Point out each leukocyte.
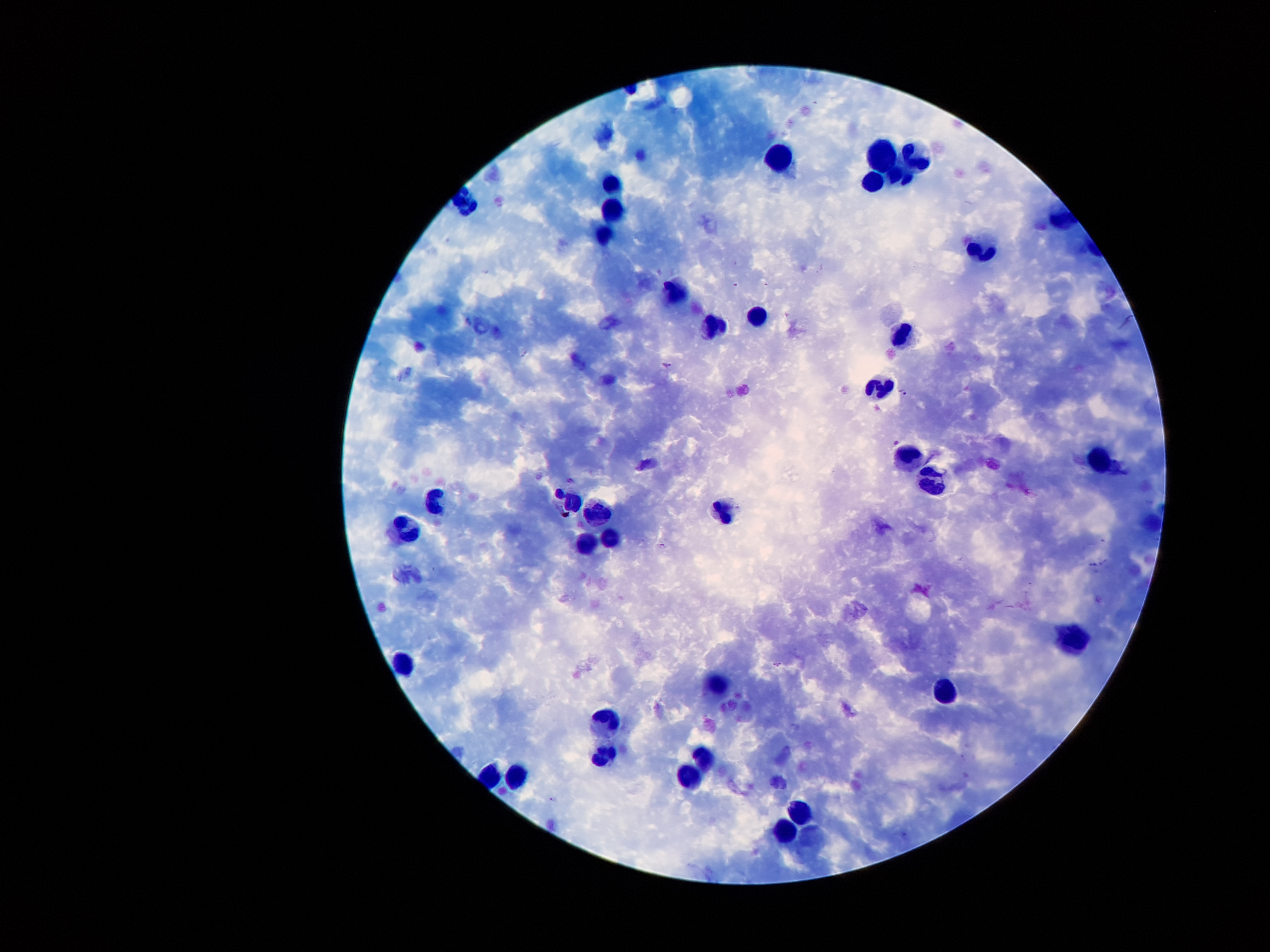

Approximate object centers, in pixels from the top-left corner.
Leukocytes: (x=883, y=155), (x=915, y=156), (x=777, y=163), (x=901, y=175), (x=873, y=180), (x=610, y=182), (x=614, y=212), (x=606, y=235), (x=983, y=251), (x=675, y=295), (x=757, y=318), (x=715, y=323), (x=903, y=337), (x=879, y=388), (x=908, y=455), (x=1094, y=459), (x=931, y=483), (x=435, y=499), (x=571, y=501), (x=723, y=505), (x=595, y=508), (x=408, y=531), (x=611, y=538), (x=587, y=546), (x=1072, y=638), (x=408, y=666), (x=719, y=686), (x=946, y=689), (x=605, y=726), (x=604, y=755), (x=700, y=756), (x=689, y=777), (x=516, y=780), (x=799, y=813), (x=787, y=831).

malaria parasite locations = (x=669, y=366), (x=905, y=390), (x=664, y=546), (x=776, y=665), (x=553, y=800)
magnification = 100x
field of view = single
preparation = thick peripheral-blood smear
capture = smartphone camera through the microscope eyepiece
image size = 1270×952 pixels
stain = Giemsa
patient malaria status = positive for Plasmodium falciparum